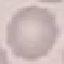

Malaria status: uninfected. Giemsa-stained preparation. Acquired by smartphone through the microscope eyepiece. Thin smear of blood. Automatically extracted cell patch, resized to 64 × 64 pixels.